Give the extent of all uninfected red blood cells.
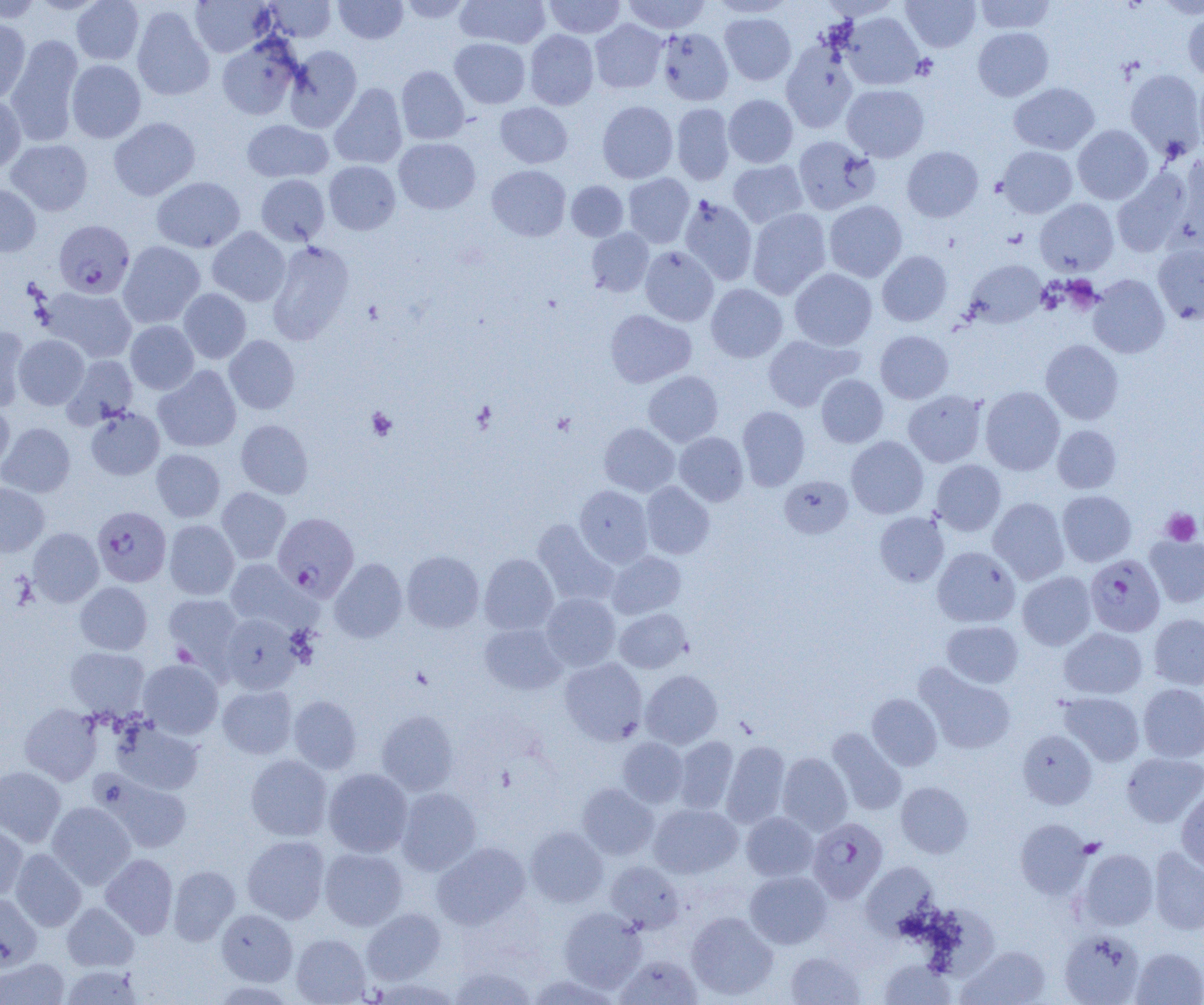
Approximate bounding boxes as (x1,y1)-(x2,y2) corner pairs in pixels.
Uninfected red blood cells: (0,0)-(43,23), (28,0)-(106,15), (71,0)-(144,65), (190,0)-(274,57), (264,0)-(336,42), (333,0)-(408,44), (399,0)-(473,23), (456,0)-(550,49), (543,0)-(625,38), (622,0)-(711,34), (710,0)-(796,18), (819,0)-(900,20), (902,0)-(980,52), (974,0)-(1056,33), (132,6)-(215,101), (1182,9)-(1204,82), (841,12)-(923,90), (720,13)-(796,85), (0,18)-(31,104), (590,20)-(667,93), (973,27)-(1053,101), (656,28)-(733,105), (524,30)-(599,110), (5,35)-(84,146), (217,35)-(302,120), (450,38)-(530,108), (781,42)-(858,133), (285,45)-(362,132), (66,59)-(146,143), (396,66)-(469,144), (1125,69)-(1204,158), (1195,74)-(1204,156), (329,83)-(407,169), (1009,83)-(1099,155), (842,84)-(929,162), (723,94)-(798,168), (0,96)-(25,175), (597,101)-(678,183), (495,102)-(573,168), (671,103)-(735,185), (109,117)-(200,201), (241,120)-(333,183), (1073,125)-(1153,204), (793,136)-(880,215), (394,137)-(481,214), (6,139)-(93,216), (902,146)-(983,222), (998,146)-(1078,218), (1174,153)-(1204,250), (728,160)-(808,228), (324,161)-(400,235), (487,165)-(571,241), (1112,169)-(1191,257), (623,173)-(695,248), (256,174)-(330,245), (151,177)-(245,253), (566,181)-(628,241), (0,184)-(41,257), (679,195)-(758,285), (1035,198)-(1118,275), (824,200)-(907,282), (747,208)-(831,299), (207,227)-(290,306), (586,228)-(654,297), (118,241)-(205,328), (266,241)-(355,344), (1153,243)-(1204,324), (640,246)-(719,325), (877,251)-(952,326), (964,260)-(1047,328), (789,268)-(877,350), (1088,275)-(1170,358), (706,284)-(787,362), (42,286)-(137,363), (179,288)-(251,364), (605,309)-(696,387), (126,320)-(199,394), (0,326)-(30,411), (875,330)-(953,403), (762,334)-(858,412), (14,335)-(89,409), (224,335)-(300,414), (1041,339)-(1124,424), (62,354)-(138,428), (153,365)-(242,452), (643,371)-(723,446), (816,374)-(888,447), (980,386)-(1064,475), (903,390)-(986,467), (0,402)-(14,474), (737,406)-(810,491), (85,407)-(164,480), (236,420)-(313,498), (0,423)-(75,497), (599,423)-(680,496), (1052,425)-(1121,493), (674,432)-(748,506), (846,436)-(928,519), (152,449)-(225,522), (930,459)-(1006,536), (779,475)-(853,538), (641,481)-(715,559), (0,483)-(49,556), (574,485)-(653,567), (217,487)-(290,563), (1057,490)-(1136,566), (988,497)-(1069,584), (875,512)-(949,587), (532,519)-(618,607), (164,520)-(239,600), (28,528)-(104,606), (1145,535)-(1204,607), (932,547)-(1020,627), (402,550)-(484,632), (606,551)-(686,619), (479,553)-(558,634), (225,558)-(308,631), (329,558)-(407,643), (1017,572)-(1096,650), (75,582)-(152,655), (163,593)-(244,670), (541,593)-(620,671), (615,608)-(691,674), (220,613)-(301,694), (1149,613)-(1204,689), (942,621)-(1023,688), (479,622)-(566,694), (1059,627)-(1147,699), (65,647)-(149,717), (560,658)-(648,745), (138,659)-(223,738), (914,662)-(1016,755), (641,670)-(723,748), (1137,683)-(1204,762), (217,684)-(297,759), (1059,692)-(1144,766), (867,693)-(942,770), (288,695)-(362,774), (20,704)-(102,785), (377,710)-(459,795), (112,719)-(204,795), (827,728)-(907,815), (1017,729)-(1097,809), (674,736)-(739,813), (618,737)-(688,807), (722,740)-(790,828), (1121,752)-(1204,826), (777,753)-(852,835), (246,754)-(332,841), (0,766)-(66,847), (323,768)-(413,857), (95,773)-(193,853), (896,781)-(973,858), (577,783)-(658,859), (396,787)-(482,875), (1176,790)-(1204,872), (47,801)-(135,889), (648,803)-(742,878), (741,812)-(819,881), (1015,819)-(1091,899), (0,821)-(28,902), (525,826)-(608,907), (241,835)-(330,924), (432,841)-(531,929), (1149,845)-(1204,935), (10,848)-(86,931), (320,848)-(407,930), (1077,848)-(1159,930), (101,853)-(178,938), (605,861)-(685,933), (861,861)-(939,935), (169,865)-(241,945), (744,870)-(832,948), (0,892)-(42,970), (62,902)-(139,971), (362,907)-(445,985), (558,907)-(647,992), (216,909)-(297,986), (686,911)-(778,1000), (1059,930)-(1145,1004), (291,933)-(371,1005), (957,946)-(1050,1004), (1131,947)-(1204,1004), (785,951)-(865,1005), (615,954)-(703,1005), (0,958)-(70,1005), (879,959)-(956,1004), (60,965)-(143,1005), (449,965)-(537,1004).

Summary:
  - Platelet locations: (912,53)-(938,79), (366,407)-(397,440), (1161,508)-(1202,546), (1079,837)-(1105,858)
  - Plasmodium falciparum-infected red blood cell locations: (54,220)-(134,298), (91,506)-(171,587), (273,512)-(359,599), (1085,554)-(1165,636), (807,817)-(888,902)
  - Slide-level diagnosis: Plasmodium falciparum
  - Field of view: one of a larger specimen
  - Modality: optical microscopy
  - Image size: 1204×1005 pixels
  - Magnification: 1000x
  - Preparation: thin blood smear